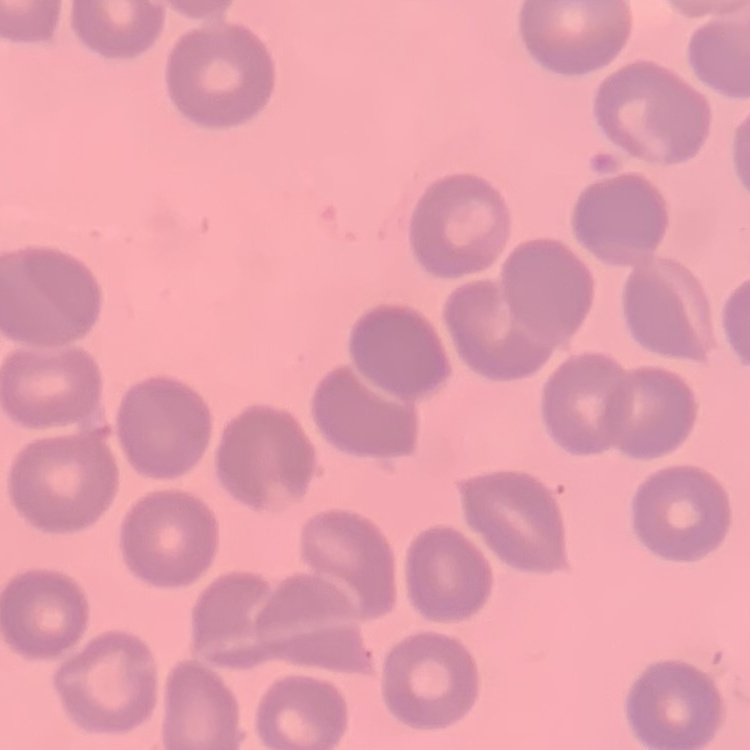
Summary:
  - Red blood cell morphology: no rouleaux formation
  - Preparation: thin blood film
  - Image type: square crop of a larger photomicrograph
  - Stain: Field's or Giemsa